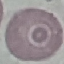

Summary:
  - Malaria status: uninfected
  - Capture: smartphone through the microscope eyepiece
  - Stain: Giemsa
  - Image type: automatically extracted cell patch, resized to 64 × 64 pixels
  - Preparation: thin smear